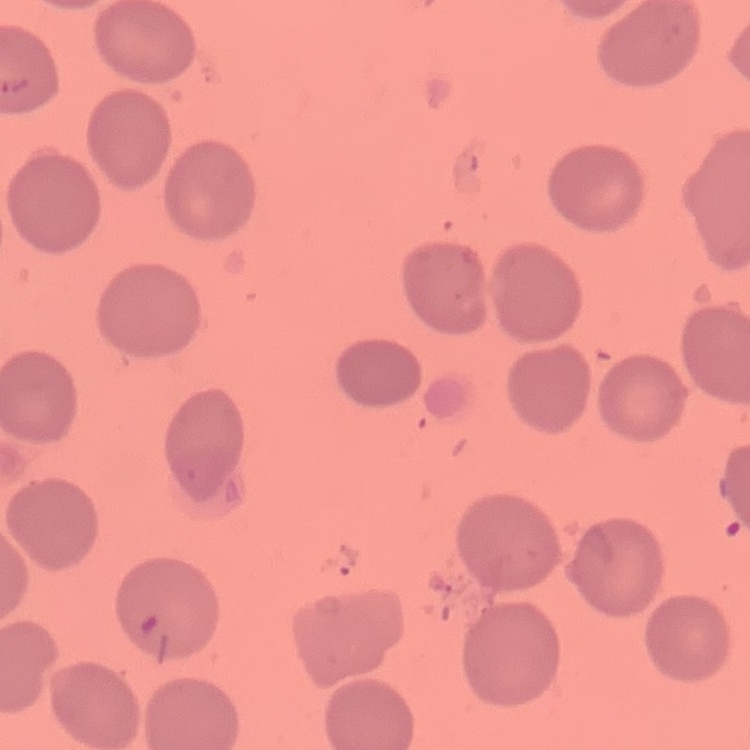

{
  "red_blood_cell_morphology": "no rouleaux formation",
  "image_type": "one tile cut from a larger photomicrograph",
  "preparation": "thin blood smear",
  "stain": "Field's or Giemsa"
}